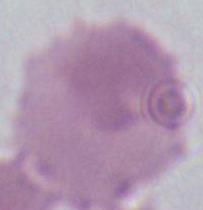

{
  "magnification": "1000x",
  "modality": "micrograph",
  "identification": "red blood cell"
}